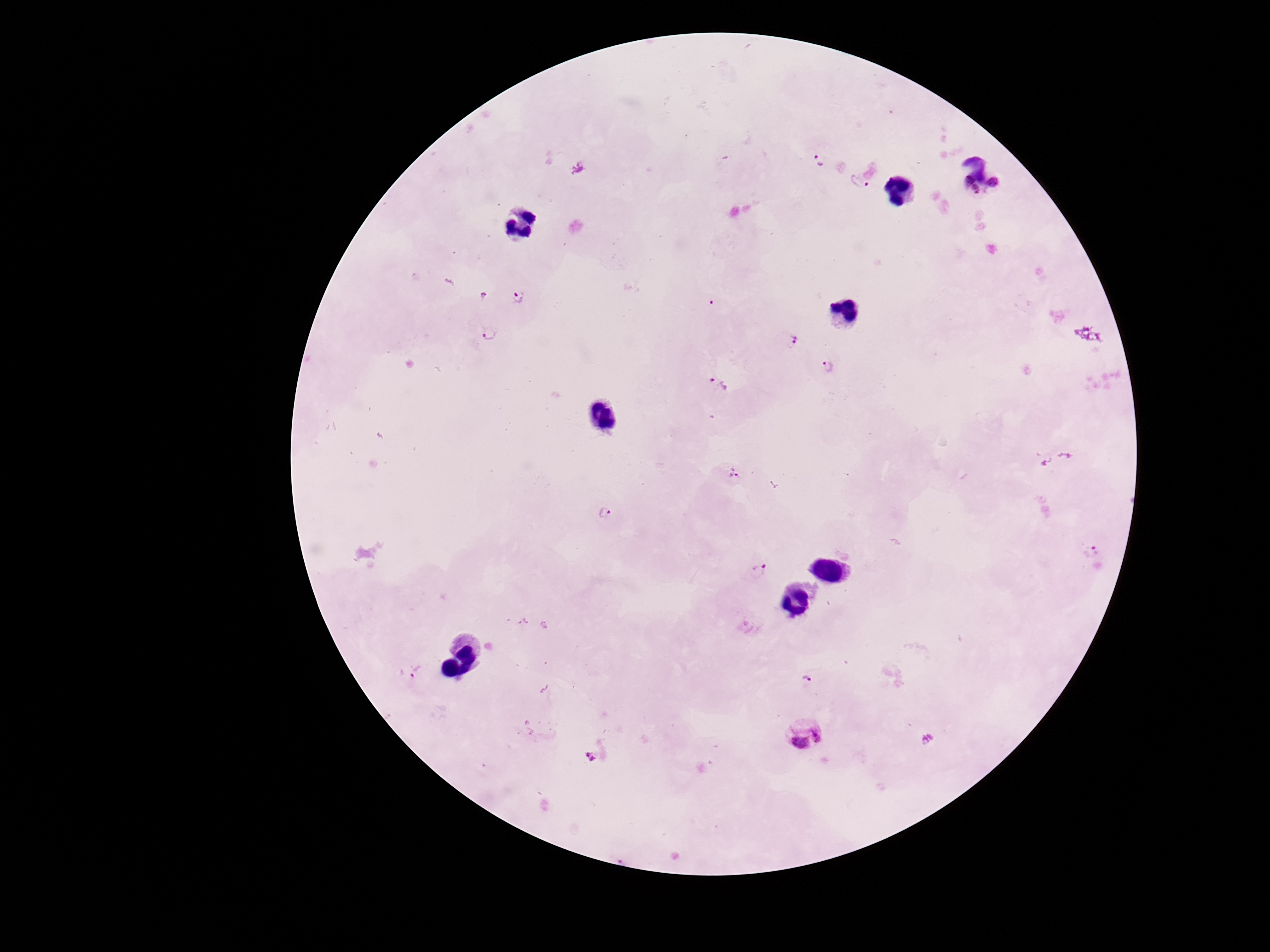

Approximate centers as {x, y} in pixels. Plasmodium parasite locations: {820, 159}, {860, 181}, {983, 186}, {518, 297}, {489, 334}, {788, 338}, {829, 368}, {719, 384}, {732, 473}, {604, 513}, {1092, 552}, {759, 570}, {416, 672}, {806, 678}, {804, 732}, {590, 756}. Image is 1270×952 pixels. Giemsa-stained preparation. Patient malaria status: infected. Smartphone photograph taken through the microscope eyepiece. 100x magnification. Thick blood film. One field from this slide.